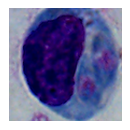 Photomicrograph. A leukocyte is seen. Captured at 1000x magnification.